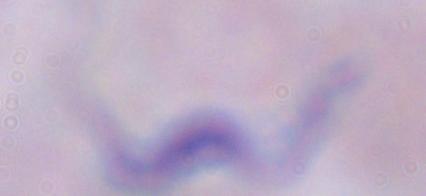

{
  "modality": "photomicrograph",
  "magnification": "1000x",
  "identification": "trypanosome"
}